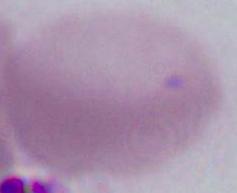

1000x magnification. An erythrocyte is seen. Micrograph.